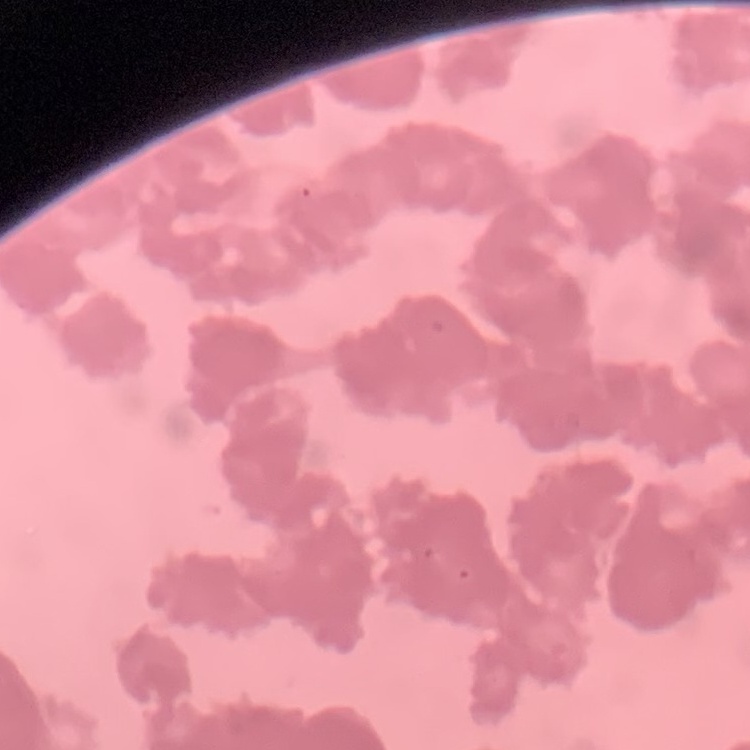
red blood cell morphology = rouleaux formation
image type = square crop of a larger photomicrograph
preparation = thin peripheral smear
stain = Field's or Giemsa